Classify this cell by malaria status.
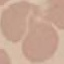

Uninfected.

Summary:
  - Stain: Giemsa
  - Preparation: thin smear
  - Image type: automatically extracted cell patch, resized to 64 × 64 pixels
  - Capture: smartphone through the microscope eyepiece